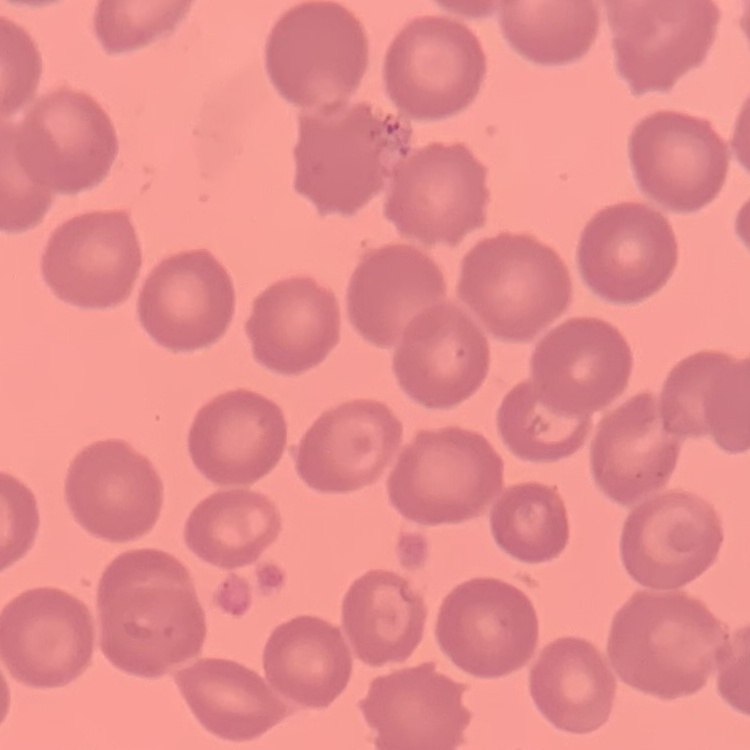

Summary:
  - Erythrocyte morphology: no rouleaux formation
  - Preparation: thin blood smear
  - Stain: Field's or Giemsa
  - Image type: square crop of a larger photomicrograph